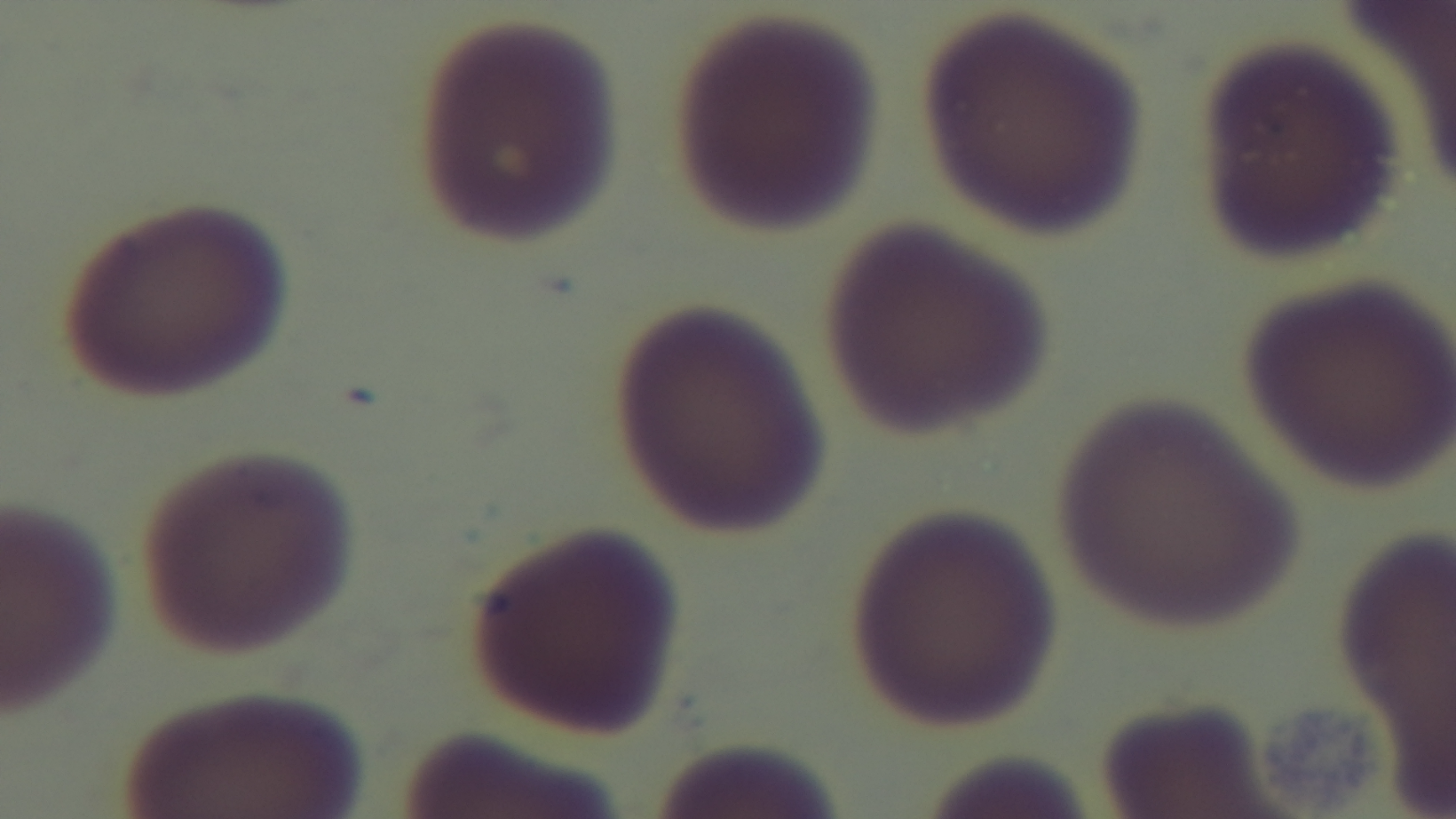

malaria status = uninfected
modality = light microscopy
capture = mounted 4K digital camera
field of view = one from the slide
stain = Giemsa
objective = 100x oil immersion
preparation = thin blood film